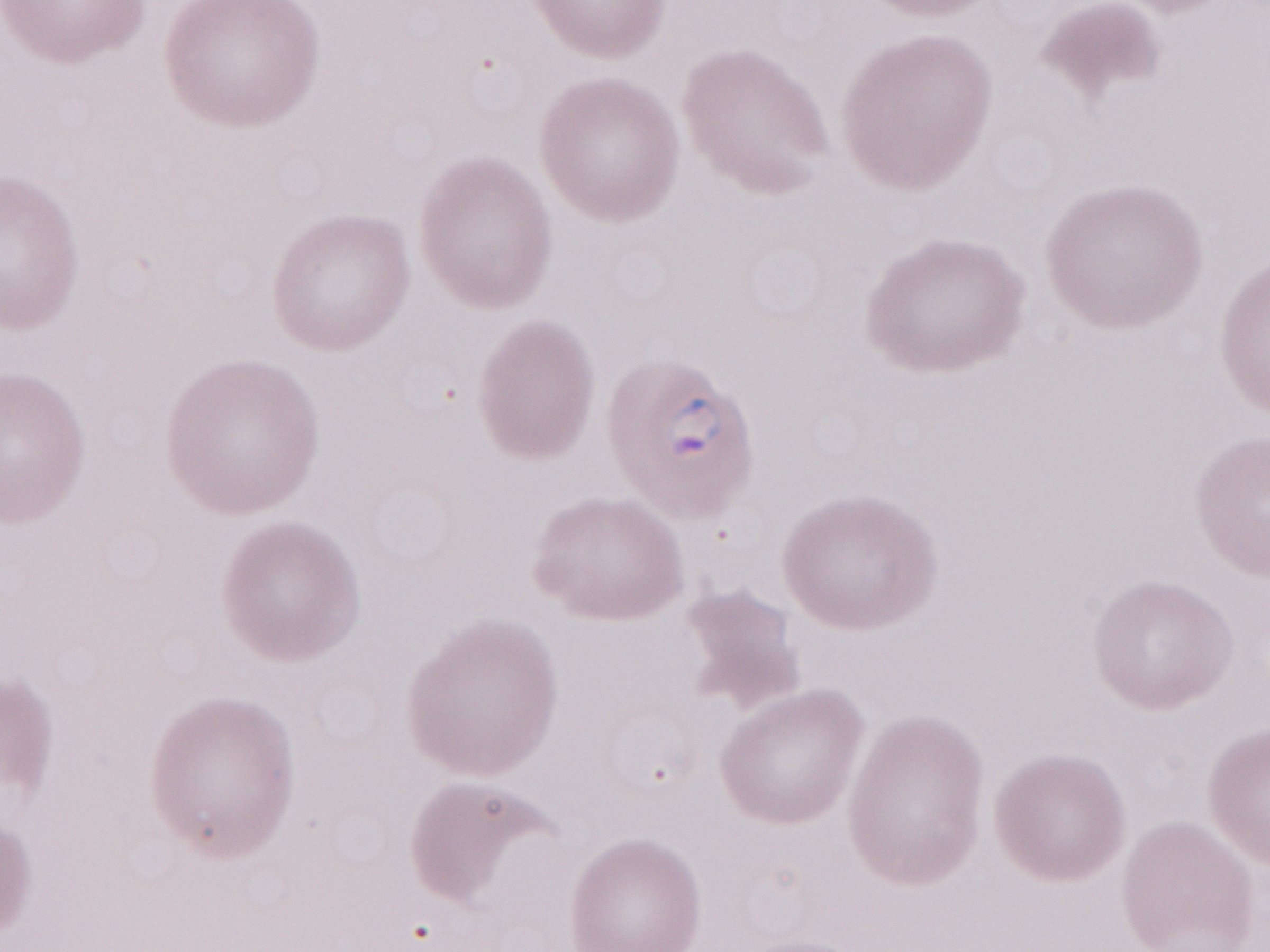

Olympus BX43 microscope, Olympus DP73 camera. Patient-level malaria diagnosis: positive. May-Grünwald-Giemsa stain. One field of this slide. 1,000x magnification. Thin peripheral-blood smear. Image is 1270×952 pixels.